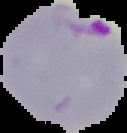
Result: malaria parasites detected. Cell region segmented out of the field of view; the surrounding area is masked to black. Image is 127×133 pixels. From a thin blood film.